Give the extent of all Plasmodium ovale-infected red blood cells.
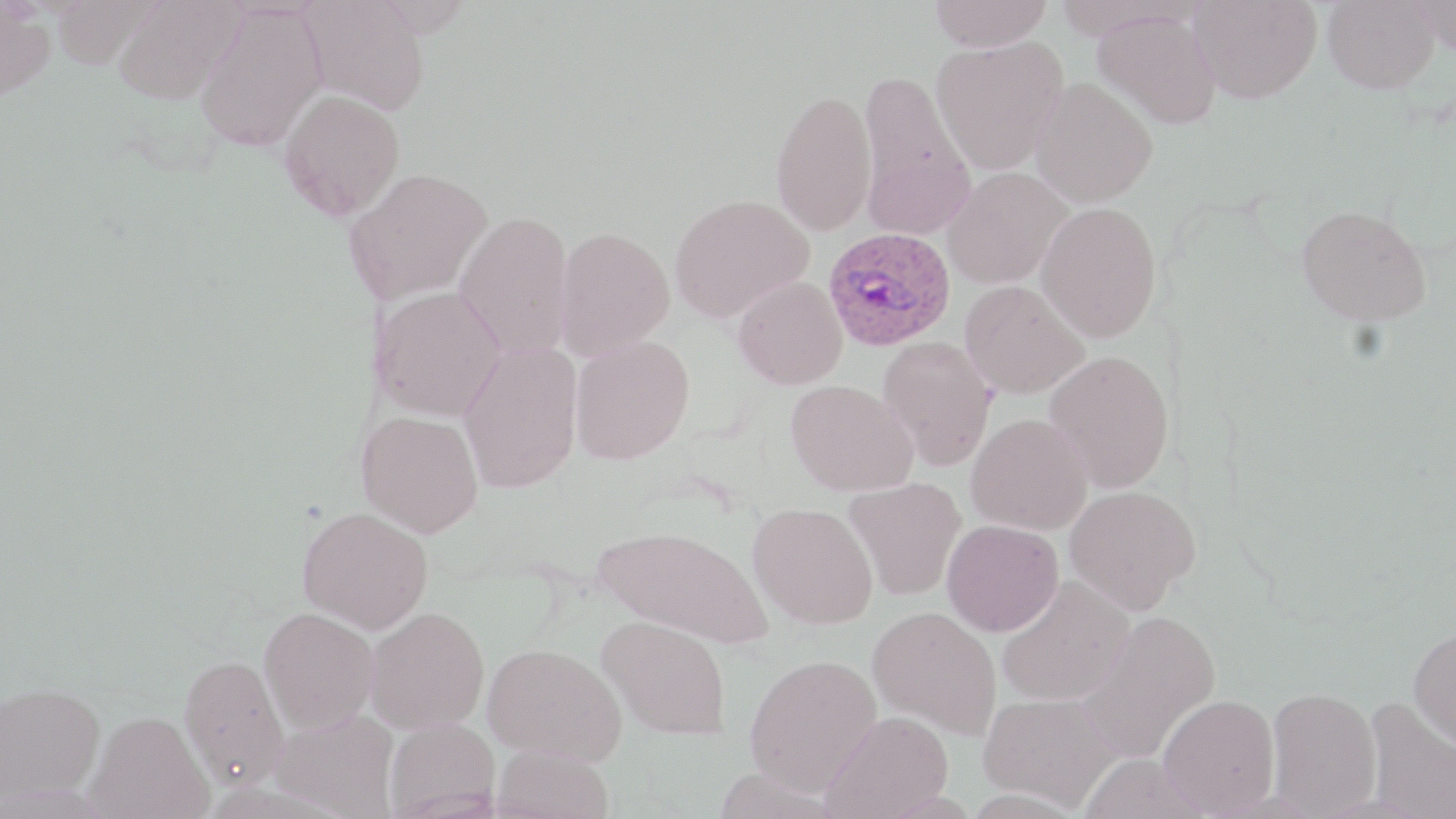

Approximate bounding boxes as named x1/y1/x2/y2 corners in pixels.
Plasmodium ovale-infected red blood cells: (x1=822, y1=226, x2=955, y2=351).

Summary:
  - Uninfected red blood cell locations: (x1=113, y1=0, x2=244, y2=104), (x1=299, y1=0, x2=432, y2=116), (x1=929, y1=0, x2=1052, y2=51), (x1=1189, y1=0, x2=1321, y2=104), (x1=1323, y1=0, x2=1440, y2=94), (x1=1412, y1=0, x2=1455, y2=58), (x1=0, y1=2, x2=56, y2=102), (x1=193, y1=4, x2=327, y2=152), (x1=1094, y1=9, x2=1221, y2=129), (x1=930, y1=36, x2=1068, y2=174), (x1=857, y1=69, x2=975, y2=238), (x1=1029, y1=77, x2=1158, y2=208), (x1=770, y1=87, x2=877, y2=236), (x1=278, y1=89, x2=406, y2=219), (x1=345, y1=166, x2=494, y2=305), (x1=943, y1=167, x2=1072, y2=289), (x1=670, y1=193, x2=814, y2=323), (x1=1036, y1=201, x2=1162, y2=342), (x1=1296, y1=204, x2=1432, y2=326), (x1=454, y1=210, x2=574, y2=361), (x1=554, y1=226, x2=675, y2=361), (x1=733, y1=276, x2=847, y2=389), (x1=959, y1=280, x2=1090, y2=399), (x1=370, y1=285, x2=506, y2=421), (x1=569, y1=334, x2=695, y2=465), (x1=877, y1=337, x2=996, y2=471), (x1=458, y1=342, x2=583, y2=494), (x1=1044, y1=349, x2=1175, y2=493), (x1=786, y1=379, x2=918, y2=496), (x1=356, y1=410, x2=484, y2=538), (x1=967, y1=414, x2=1093, y2=535), (x1=843, y1=477, x2=966, y2=600), (x1=1064, y1=484, x2=1201, y2=614), (x1=748, y1=502, x2=878, y2=629), (x1=297, y1=506, x2=433, y2=633), (x1=942, y1=520, x2=1064, y2=636), (x1=594, y1=523, x2=773, y2=649), (x1=996, y1=576, x2=1134, y2=707), (x1=364, y1=606, x2=490, y2=734), (x1=867, y1=606, x2=1002, y2=739), (x1=259, y1=607, x2=379, y2=733), (x1=1078, y1=610, x2=1221, y2=763), (x1=597, y1=615, x2=732, y2=741), (x1=1408, y1=624, x2=1456, y2=751), (x1=483, y1=642, x2=627, y2=764), (x1=179, y1=652, x2=290, y2=790), (x1=744, y1=653, x2=883, y2=796), (x1=1, y1=681, x2=106, y2=805), (x1=1266, y1=686, x2=1382, y2=816), (x1=979, y1=691, x2=1121, y2=810), (x1=1157, y1=694, x2=1280, y2=816), (x1=1363, y1=696, x2=1456, y2=819), (x1=270, y1=708, x2=399, y2=818), (x1=821, y1=710, x2=954, y2=818), (x1=86, y1=711, x2=214, y2=818), (x1=384, y1=718, x2=500, y2=818), (x1=492, y1=743, x2=615, y2=819), (x1=1077, y1=753, x2=1210, y2=818)
  - Slide-level diagnosis: Plasmodium ovale
  - Modality: optical microscopy
  - Field of view: single
  - Magnification: 1000x
  - Image size: 1456×819 pixels
  - Preparation: thin blood film
  - Stain: May-Grünwald-Giemsa